Classify this cell by malaria status.
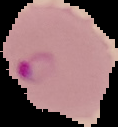

It is parasitized.

Summary:
  - Image size: 118×127 pixels
  - Preparation: thin blood smear
  - Image type: segmented cell region with the area outside set to black